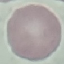

malaria status = uninfected
preparation = thin blood smear
capture = smartphone camera at the microscope eyepiece
image type = cell patch, automatically extracted from a larger field of view and resized to 64 × 64 pixels
stain = Giemsa